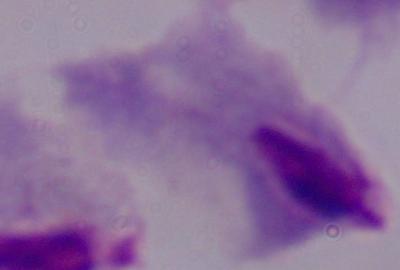 1000x magnification. A trichomonad is seen. Photomicrograph.